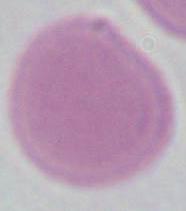
An erythrocyte is shown. Micrograph. 1000x magnification.